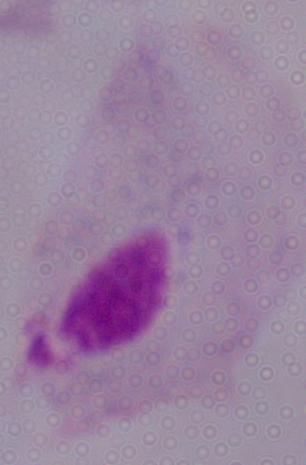
Summary:
  - Magnification: 1000x
  - Modality: photomicrograph
  - Identification: trichomonad